Describe the morphology of the red blood cells.
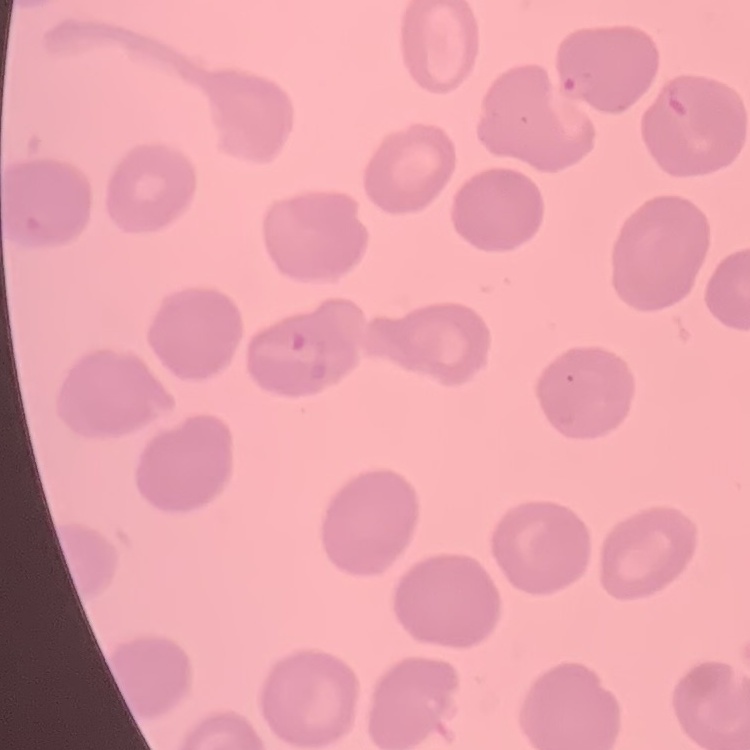
They show no rouleaux formation.

image type = square crop of a larger photomicrograph
stain = Field's or Giemsa
preparation = thin blood smear